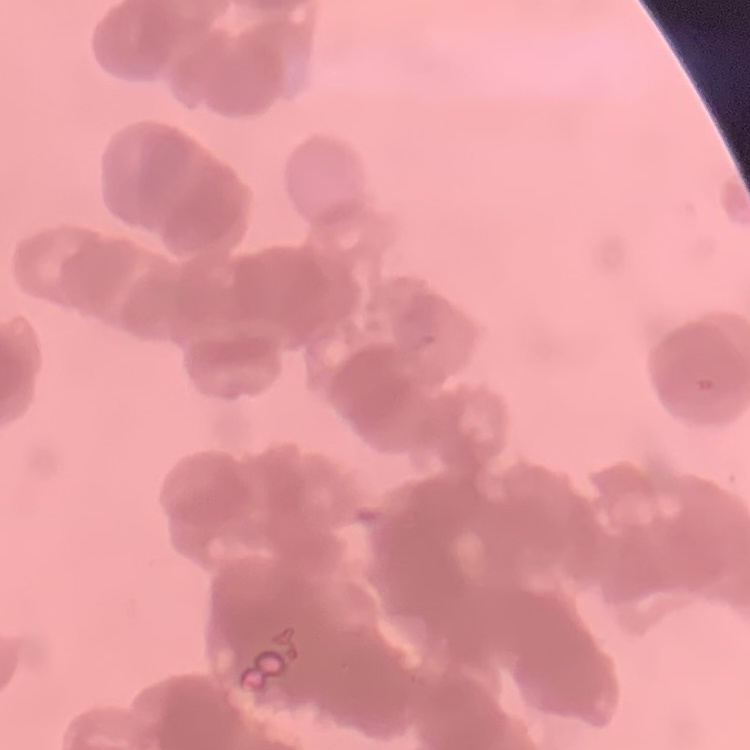
Summary:
  - Erythrocyte morphology: rouleaux formation
  - Preparation: thin blood film
  - Stain: Field's or Giemsa
  - Image type: one tile cut from a larger photomicrograph